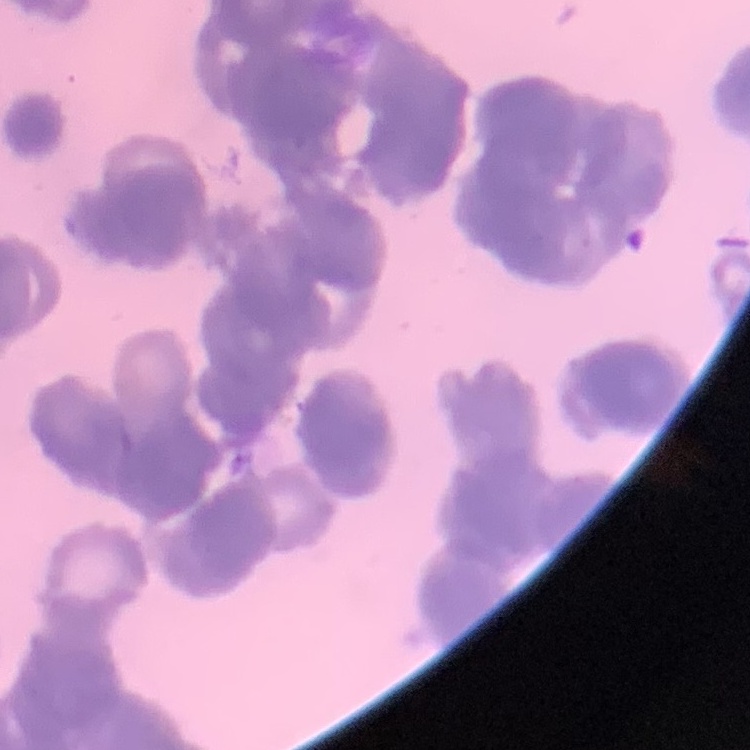
red_blood_cell_morphology: rouleaux formation
stain: Field's or Giemsa
preparation: thin blood smear
image_type: one tile cut from a larger photomicrograph